State the blood parasite species.
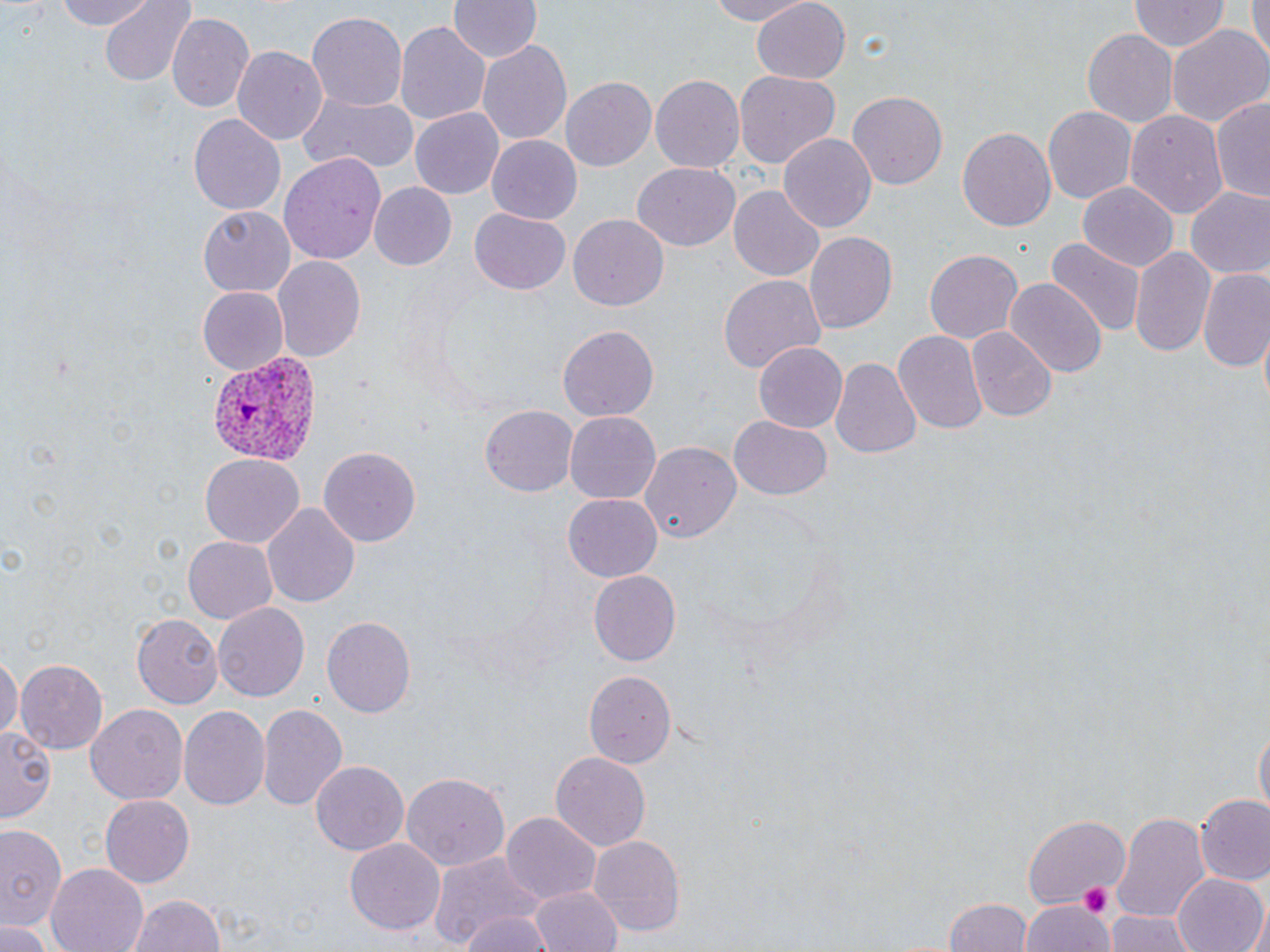

Plasmodium vivax.

Approximate bounding boxes as named x1/y1/x2/y2 corners in pixels. Plasmodium vivax-infected red blood cell locations: (x1=204, y1=353, x2=322, y2=466). Uninfected red blood cell locations: (x1=51, y1=0, x2=161, y2=30), (x1=99, y1=0, x2=196, y2=87), (x1=448, y1=0, x2=541, y2=64), (x1=702, y1=0, x2=815, y2=26), (x1=1244, y1=0, x2=1267, y2=68), (x1=749, y1=1, x2=850, y2=85), (x1=1128, y1=1, x2=1228, y2=54), (x1=459, y1=5, x2=559, y2=112), (x1=306, y1=11, x2=407, y2=112), (x1=167, y1=12, x2=254, y2=111), (x1=395, y1=20, x2=492, y2=127), (x1=1166, y1=25, x2=1269, y2=131), (x1=1082, y1=29, x2=1178, y2=128), (x1=475, y1=37, x2=571, y2=147), (x1=231, y1=43, x2=327, y2=142), (x1=734, y1=72, x2=840, y2=170), (x1=650, y1=74, x2=746, y2=173), (x1=560, y1=75, x2=656, y2=171), (x1=296, y1=89, x2=418, y2=175), (x1=847, y1=91, x2=947, y2=191), (x1=1211, y1=96, x2=1270, y2=202), (x1=1042, y1=106, x2=1135, y2=205), (x1=410, y1=108, x2=503, y2=198), (x1=1125, y1=108, x2=1230, y2=219), (x1=189, y1=113, x2=286, y2=216), (x1=958, y1=127, x2=1056, y2=232), (x1=779, y1=132, x2=877, y2=233), (x1=485, y1=136, x2=582, y2=224), (x1=279, y1=153, x2=386, y2=263), (x1=633, y1=164, x2=739, y2=250), (x1=1078, y1=180, x2=1179, y2=270), (x1=368, y1=183, x2=458, y2=273), (x1=730, y1=185, x2=823, y2=281), (x1=1185, y1=188, x2=1270, y2=281), (x1=199, y1=205, x2=295, y2=294), (x1=471, y1=209, x2=570, y2=295), (x1=566, y1=213, x2=668, y2=311), (x1=804, y1=231, x2=896, y2=336), (x1=1045, y1=238, x2=1147, y2=339), (x1=1130, y1=246, x2=1214, y2=356), (x1=925, y1=249, x2=1023, y2=347), (x1=271, y1=255, x2=368, y2=362), (x1=1197, y1=271, x2=1270, y2=371), (x1=717, y1=275, x2=824, y2=374), (x1=1006, y1=278, x2=1105, y2=382), (x1=197, y1=287, x2=290, y2=375), (x1=558, y1=324, x2=659, y2=420), (x1=966, y1=328, x2=1055, y2=422), (x1=1257, y1=328, x2=1269, y2=413), (x1=894, y1=330, x2=988, y2=436), (x1=754, y1=343, x2=847, y2=432), (x1=832, y1=357, x2=921, y2=461), (x1=482, y1=405, x2=579, y2=497), (x1=564, y1=412, x2=659, y2=504), (x1=728, y1=417, x2=832, y2=500), (x1=642, y1=442, x2=742, y2=542), (x1=319, y1=447, x2=422, y2=546), (x1=198, y1=455, x2=304, y2=548), (x1=563, y1=494, x2=660, y2=582), (x1=262, y1=502, x2=360, y2=609), (x1=182, y1=535, x2=278, y2=624), (x1=589, y1=572, x2=681, y2=663), (x1=213, y1=603, x2=309, y2=700), (x1=133, y1=614, x2=221, y2=707), (x1=322, y1=616, x2=416, y2=718), (x1=0, y1=653, x2=21, y2=744), (x1=15, y1=659, x2=110, y2=753), (x1=583, y1=669, x2=676, y2=767), (x1=258, y1=703, x2=346, y2=811), (x1=86, y1=704, x2=186, y2=806), (x1=177, y1=704, x2=270, y2=809), (x1=2, y1=726, x2=53, y2=823), (x1=1254, y1=726, x2=1268, y2=822), (x1=550, y1=750, x2=652, y2=854), (x1=310, y1=761, x2=407, y2=856), (x1=400, y1=771, x2=511, y2=872), (x1=100, y1=795, x2=193, y2=886), (x1=1196, y1=795, x2=1270, y2=886), (x1=1113, y1=810, x2=1210, y2=921), (x1=500, y1=813, x2=600, y2=901), (x1=1025, y1=813, x2=1130, y2=908), (x1=0, y1=822, x2=64, y2=933), (x1=590, y1=835, x2=685, y2=939), (x1=344, y1=839, x2=446, y2=937), (x1=429, y1=852, x2=551, y2=952), (x1=45, y1=864, x2=148, y2=952), (x1=1172, y1=874, x2=1269, y2=952), (x1=529, y1=884, x2=623, y2=952), (x1=123, y1=891, x2=229, y2=952), (x1=945, y1=897, x2=1033, y2=952), (x1=1021, y1=899, x2=1113, y2=952), (x1=450, y1=906, x2=558, y2=952), (x1=1104, y1=909, x2=1201, y2=952), (x1=0, y1=923, x2=52, y2=952). Platelet locations: (x1=1081, y1=884, x2=1112, y2=917). May-Grünwald-Giemsa stain. Image is 1270×952 pixels. Single field of view. Thin blood film. Light microscopy. Captured at 1000x magnification.